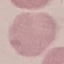
malaria status = uninfected
stain = Giemsa
capture = smartphone camera at the microscope eyepiece
image type = automatically extracted cell patch, resized to 64 × 64 pixels
preparation = thin blood film